Assess this cell for malaria.
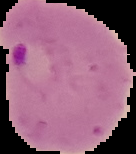
Parasitized.

Summary:
  - Image size: 136×154 pixels
  - Preparation: thin blood smear
  - Image type: segmented cell region with the area outside set to black